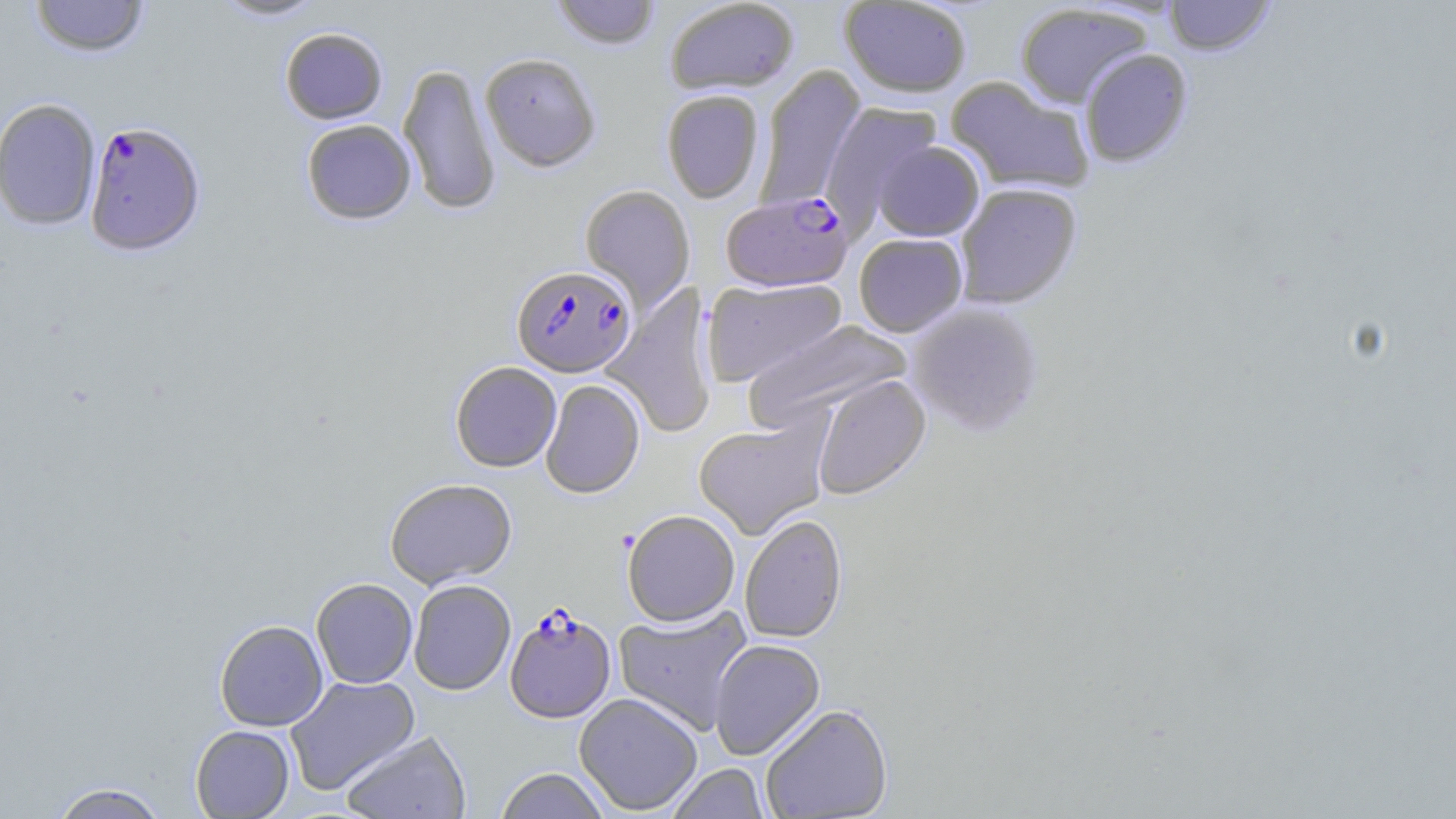
slide_level_diagnosis: Plasmodium falciparum
field_of_view: one of a larger specimen
image_size: 1456×819 pixels
preparation: thin blood film
stain: May-Grünwald-Giemsa
plasmodium_falciparum_infected_red_blood_cell_locations: 'approximate bounding boxes as named x1/y1/x2/y2 corners in pixels: (x1=84, y1=120, x2=205, y2=256), (x1=721, y1=191, x2=854, y2=293), (x1=512, y1=264, x2=636, y2=377), (x1=505, y1=607, x2=616, y2=723)'
magnification: 1000x
uninfected_red_blood_cell_locations: 'approximate bounding boxes as named x1/y1/x2/y2 corners in pixels: (x1=29, y1=0, x2=150, y2=58), (x1=211, y1=0, x2=328, y2=22), (x1=550, y1=0, x2=662, y2=50), (x1=664, y1=0, x2=799, y2=95), (x1=839, y1=0, x2=972, y2=98), (x1=1163, y1=0, x2=1275, y2=58), (x1=1015, y1=3, x2=1151, y2=108), (x1=279, y1=27, x2=388, y2=124), (x1=1079, y1=49, x2=1193, y2=169), (x1=480, y1=52, x2=601, y2=172), (x1=398, y1=62, x2=500, y2=216), (x1=756, y1=65, x2=866, y2=210), (x1=946, y1=77, x2=1095, y2=195), (x1=661, y1=90, x2=764, y2=204), (x1=0, y1=98, x2=102, y2=231), (x1=821, y1=101, x2=943, y2=230), (x1=301, y1=119, x2=417, y2=225), (x1=871, y1=140, x2=985, y2=241), (x1=580, y1=184, x2=695, y2=313), (x1=956, y1=184, x2=1082, y2=309), (x1=854, y1=234, x2=968, y2=338), (x1=702, y1=277, x2=848, y2=387), (x1=603, y1=284, x2=718, y2=440), (x1=907, y1=303, x2=1045, y2=437), (x1=743, y1=319, x2=914, y2=431), (x1=450, y1=361, x2=562, y2=472), (x1=811, y1=375, x2=931, y2=500), (x1=540, y1=379, x2=645, y2=499), (x1=693, y1=417, x2=831, y2=539), (x1=385, y1=478, x2=517, y2=588), (x1=622, y1=509, x2=740, y2=627), (x1=740, y1=514, x2=848, y2=643), (x1=311, y1=578, x2=418, y2=688), (x1=408, y1=579, x2=516, y2=695), (x1=613, y1=604, x2=754, y2=735), (x1=214, y1=620, x2=328, y2=731), (x1=709, y1=639, x2=825, y2=761), (x1=285, y1=675, x2=420, y2=794), (x1=574, y1=693, x2=703, y2=816), (x1=760, y1=704, x2=894, y2=819), (x1=190, y1=725, x2=294, y2=818), (x1=340, y1=730, x2=472, y2=819), (x1=666, y1=763, x2=771, y2=819), (x1=493, y1=767, x2=612, y2=819), (x1=48, y1=782, x2=170, y2=819)'
modality: optical microscopy